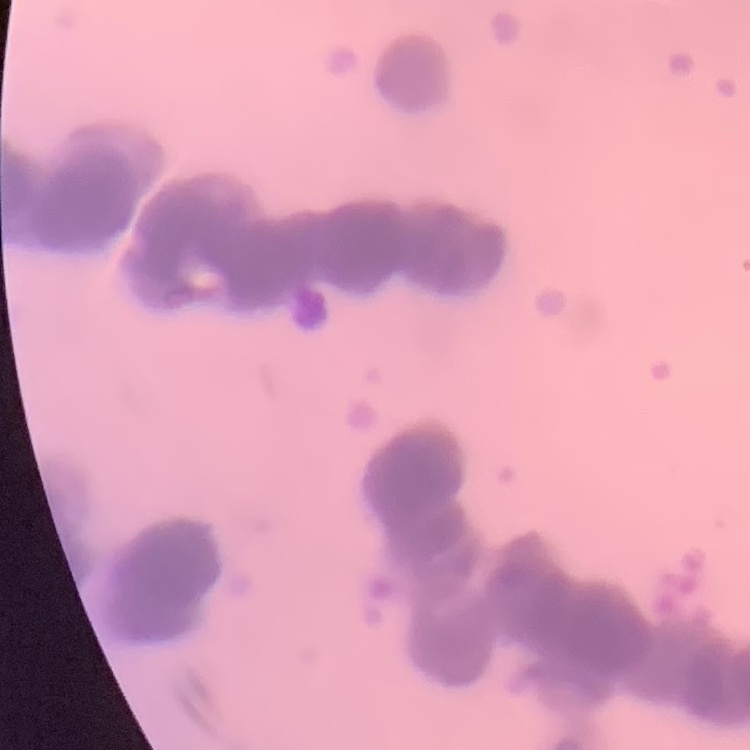
red_blood_cell_morphology: rouleaux formation
image_type: one tile cut from a larger photomicrograph
preparation: thin blood smear
stain: Field's or Giemsa